Comment on the morphology of the erythrocytes.
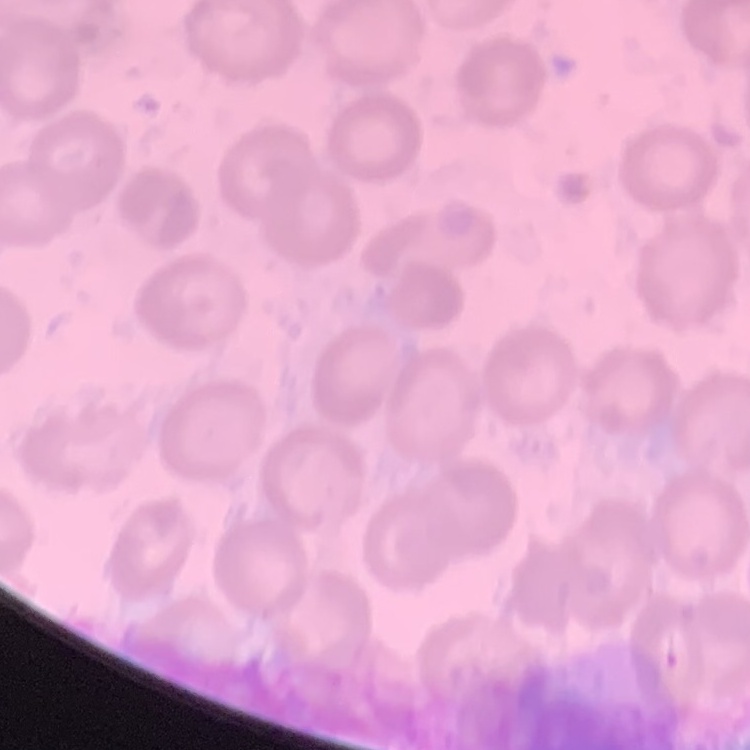
No rouleaux formation.

One tile cut from a larger photomicrograph. Thin blood smear. Stained with either Field's or Giemsa.